Locate every Plasmodium parasite.
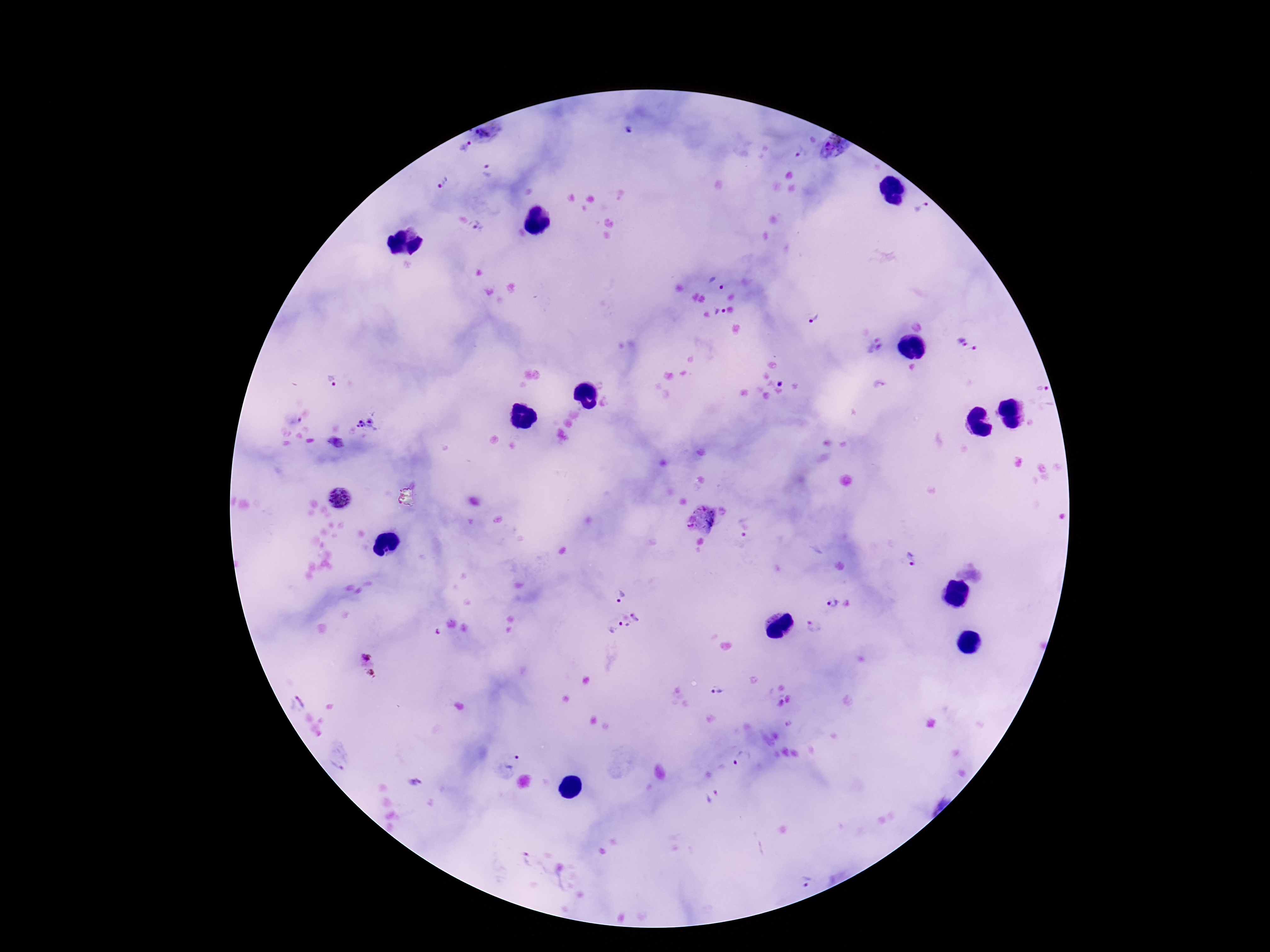

Approximate object centers, in pixels from the top-left corner.
Plasmodium parasites: (x=628, y=131), (x=490, y=136), (x=464, y=147), (x=833, y=147), (x=800, y=153), (x=487, y=171), (x=442, y=182), (x=920, y=206), (x=477, y=228), (x=718, y=284), (x=720, y=311), (x=812, y=318), (x=968, y=345), (x=873, y=346), (x=332, y=381), (x=878, y=384), (x=1042, y=390), (x=365, y=426), (x=336, y=444), (x=339, y=498), (x=703, y=520), (x=743, y=526), (x=912, y=559), (x=619, y=595), (x=831, y=603), (x=622, y=622), (x=813, y=626), (x=369, y=666), (x=717, y=691), (x=742, y=759), (x=513, y=761), (x=415, y=783), (x=713, y=794), (x=523, y=859), (x=804, y=876).

Patient malaria status: infected. 100x magnification. Single field of view. Giemsa-stained preparation. Image is 1270×952 pixels. Thick blood film. Smartphone photograph taken through the microscope eyepiece.